Name the blood parasite species.
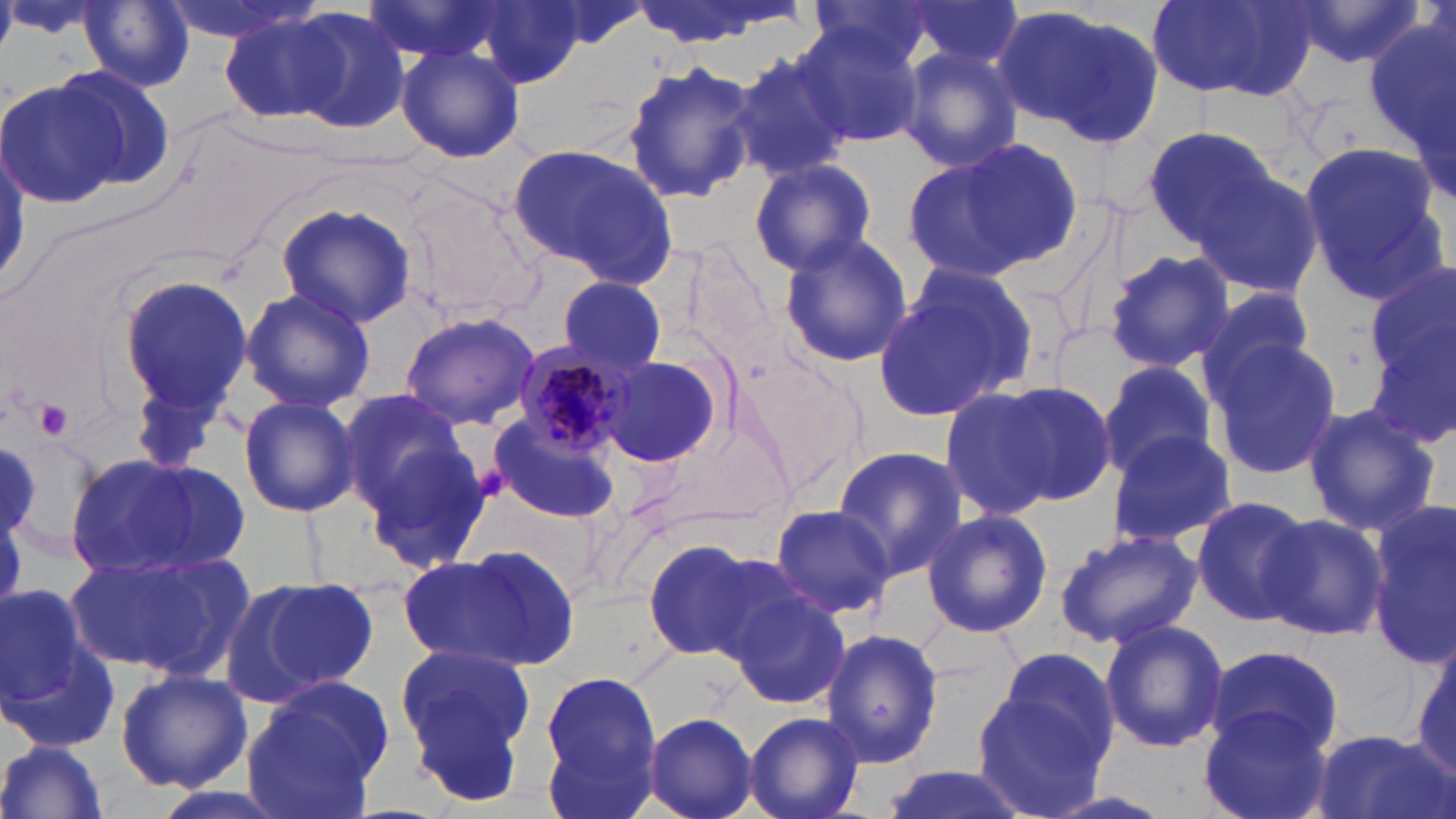

Plasmodium malariae.

Summary:
  - Coordinate format: approximate bounding boxes as named x1/y1/x2/y2 corners in pixels
  - Uninfected red blood cell locations: (x1=156, y1=0, x2=319, y2=47), (x1=469, y1=0, x2=588, y2=89), (x1=627, y1=0, x2=806, y2=49), (x1=803, y1=0, x2=944, y2=73), (x1=896, y1=0, x2=1027, y2=79), (x1=1290, y1=0, x2=1429, y2=71), (x1=80, y1=1, x2=196, y2=92), (x1=1148, y1=1, x2=1315, y2=101), (x1=532, y1=3, x2=648, y2=52), (x1=995, y1=6, x2=1157, y2=143), (x1=216, y1=8, x2=345, y2=124), (x1=283, y1=8, x2=412, y2=134), (x1=1359, y1=19, x2=1455, y2=152), (x1=793, y1=22, x2=923, y2=149), (x1=395, y1=44, x2=525, y2=164), (x1=896, y1=45, x2=1025, y2=174), (x1=726, y1=52, x2=851, y2=180), (x1=620, y1=57, x2=758, y2=205), (x1=49, y1=63, x2=178, y2=193), (x1=0, y1=77, x2=126, y2=211), (x1=1142, y1=122, x2=1284, y2=250), (x1=905, y1=139, x2=1078, y2=281), (x1=508, y1=143, x2=677, y2=286), (x1=1300, y1=143, x2=1453, y2=306), (x1=748, y1=158, x2=877, y2=275), (x1=1190, y1=165, x2=1325, y2=300), (x1=274, y1=202, x2=417, y2=328), (x1=776, y1=234, x2=915, y2=368), (x1=1104, y1=249, x2=1235, y2=373), (x1=1362, y1=262, x2=1456, y2=399), (x1=873, y1=268, x2=1034, y2=422), (x1=115, y1=273, x2=254, y2=423), (x1=557, y1=276, x2=667, y2=375), (x1=239, y1=287, x2=375, y2=414), (x1=1193, y1=288, x2=1318, y2=397), (x1=398, y1=312, x2=540, y2=429), (x1=1365, y1=317, x2=1456, y2=456), (x1=1206, y1=332, x2=1344, y2=484), (x1=597, y1=354, x2=727, y2=467), (x1=1095, y1=360, x2=1219, y2=480), (x1=1000, y1=380, x2=1117, y2=505), (x1=937, y1=386, x2=1060, y2=521), (x1=338, y1=393, x2=474, y2=516), (x1=237, y1=396, x2=361, y2=517), (x1=1300, y1=402, x2=1440, y2=537), (x1=489, y1=415, x2=622, y2=523), (x1=1105, y1=430, x2=1238, y2=548), (x1=359, y1=436, x2=494, y2=575), (x1=0, y1=439, x2=41, y2=545), (x1=831, y1=445, x2=968, y2=579), (x1=66, y1=452, x2=247, y2=581), (x1=1190, y1=494, x2=1316, y2=626), (x1=1365, y1=500, x2=1455, y2=665), (x1=767, y1=503, x2=897, y2=619), (x1=921, y1=507, x2=1053, y2=638), (x1=1259, y1=514, x2=1388, y2=644), (x1=1054, y1=527, x2=1203, y2=649), (x1=641, y1=537, x2=783, y2=662), (x1=68, y1=545, x2=253, y2=678), (x1=403, y1=545, x2=578, y2=672), (x1=226, y1=574, x2=378, y2=705), (x1=0, y1=582, x2=102, y2=728), (x1=723, y1=583, x2=850, y2=711), (x1=1099, y1=617, x2=1229, y2=754), (x1=820, y1=630, x2=944, y2=768), (x1=1405, y1=639, x2=1456, y2=782), (x1=394, y1=643, x2=539, y2=803), (x1=1205, y1=644, x2=1349, y2=758), (x1=114, y1=668, x2=254, y2=792), (x1=540, y1=669, x2=662, y2=804), (x1=971, y1=681, x2=1114, y2=819), (x1=239, y1=684, x2=387, y2=819), (x1=1199, y1=706, x2=1333, y2=819), (x1=742, y1=711, x2=865, y2=819), (x1=642, y1=712, x2=758, y2=819), (x1=1307, y1=730, x2=1451, y2=819), (x1=0, y1=738, x2=111, y2=819), (x1=876, y1=764, x2=1032, y2=819)
  - Platelet locations: (x1=35, y1=399, x2=73, y2=438)
  - Plasmodium malariae-infected red blood cell locations: (x1=509, y1=343, x2=638, y2=456)
  - Field of view: one of a larger specimen
  - Magnification: 1000x
  - Stain: May-Grünwald-Giemsa
  - Modality: optical microscopy
  - Image size: 1456×819 pixels
  - Preparation: thin blood smear